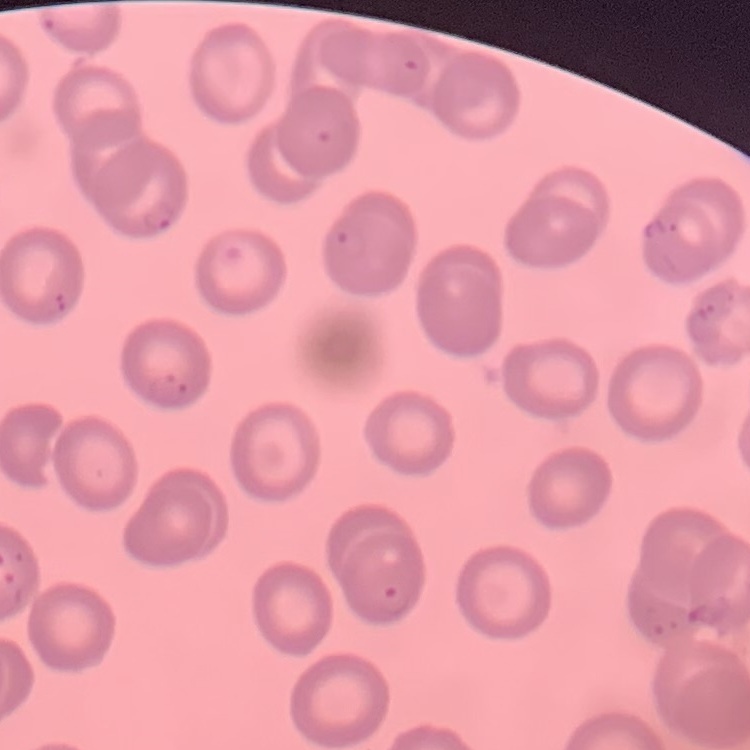

red blood cell morphology = no rouleaux formation
stain = Field's or Giemsa
preparation = thin peripheral smear
image type = square crop of a larger photomicrograph